Identify the cell.
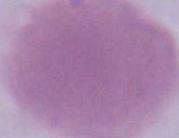

This is an erythrocyte.

Micrograph. Captured at 1000x magnification.